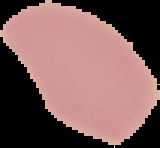
malaria status = uninfected
image size = 160×148 pixels
image type = segmented cell region on a black background
preparation = thin blood film